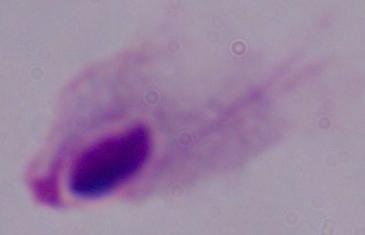
Summary:
  - Identification: trichomonad
  - Magnification: 1000x
  - Modality: micrograph